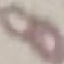
Summary:
  - Malaria status: uninfected
  - Image type: automatically extracted cell patch, resized to 64 × 64 pixels
  - Stain: Giemsa
  - Capture: smartphone through the microscope eyepiece
  - Preparation: thin blood smear